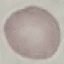

result = negative for malaria parasites
stain = Giemsa
capture = smartphone camera at the microscope eyepiece
image type = automatically extracted cell patch, resized to 64 × 64 pixels
preparation = thin smear